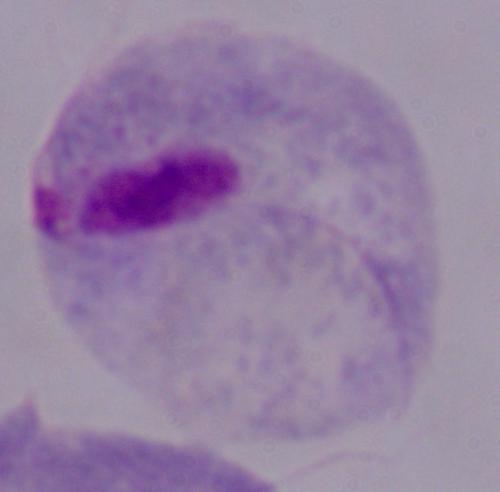
Micrograph. A trichomonad is shown. 1000x magnification.